State which cell type is depicted.
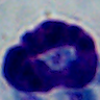

A leukocyte.

1000x magnification. Micrograph.